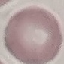

Summary:
  - Result: negative for malaria parasites
  - Stain: Giemsa
  - Image type: automatically extracted cell patch, resized to 64 × 64 pixels
  - Capture: smartphone through the microscope eyepiece
  - Preparation: thin blood smear